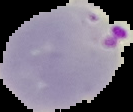

Image is 133×112 pixels. From a thin blood smear. Malaria status: parasitized. The area outside the segmented cell region is set to black.